Give the extent of all Plasmodium falciparum-infected red blood cells.
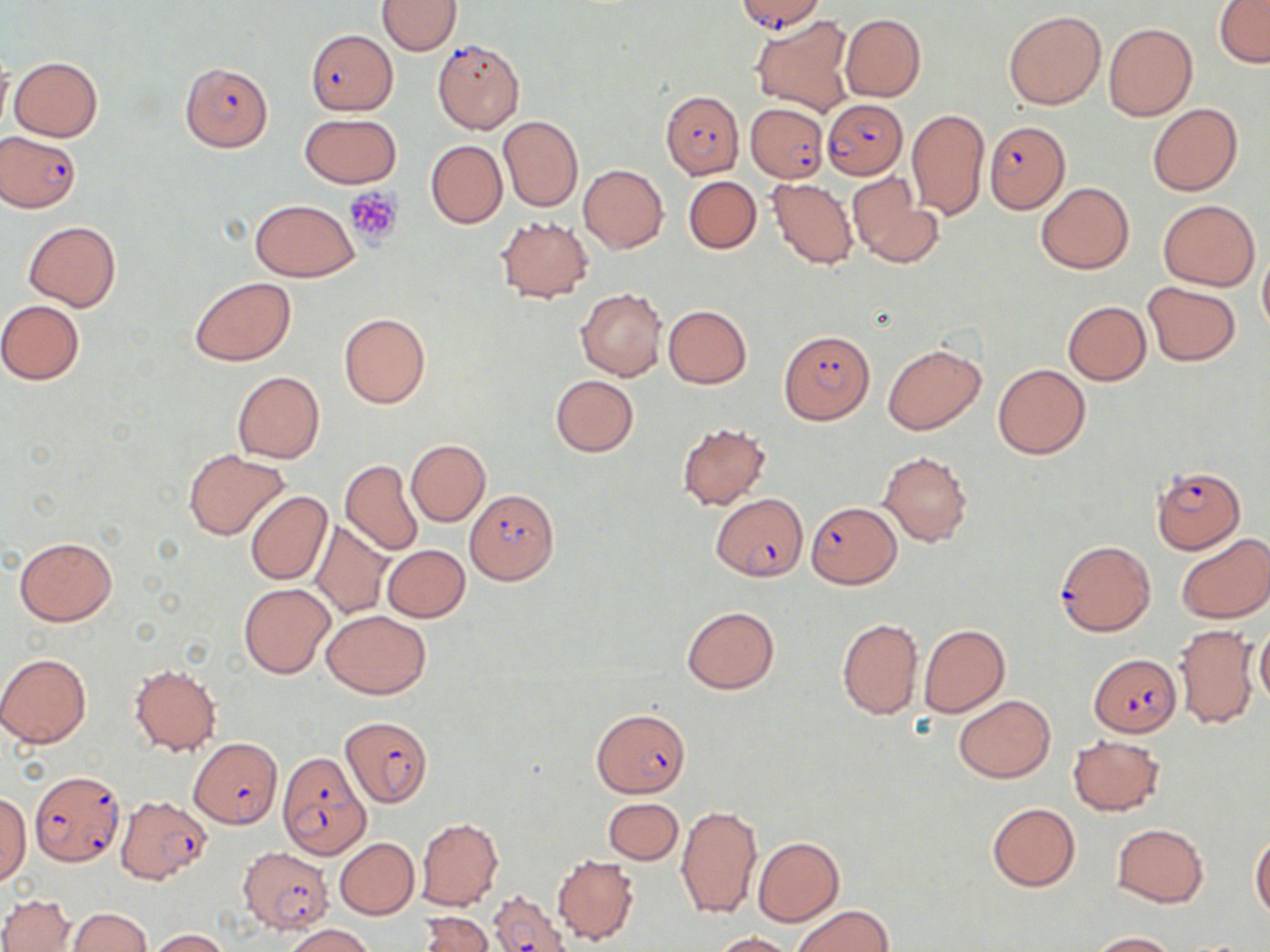

Approximate bounding boxes as [x1, y1, x2, y2] in pixels.
Plasmodium falciparum-infected red blood cells: [735, 0, 824, 34], [307, 29, 396, 115], [432, 37, 526, 134], [180, 62, 273, 151], [663, 89, 744, 180], [821, 98, 908, 179], [744, 102, 829, 182], [984, 120, 1070, 213], [0, 132, 82, 213], [778, 331, 874, 424], [1150, 466, 1245, 553], [464, 490, 558, 585], [710, 494, 807, 579], [806, 500, 901, 588], [1054, 540, 1155, 636], [1091, 653, 1180, 735], [590, 708, 690, 798], [340, 716, 433, 807], [189, 737, 282, 828], [276, 753, 371, 859], [28, 769, 126, 867], [115, 794, 212, 884], [237, 847, 334, 933], [487, 889, 570, 951].

Platelet locations: [344, 187, 404, 246]. Uninfected red blood cell locations: [378, 0, 460, 55], [1214, 0, 1269, 68], [1004, 11, 1106, 109], [839, 13, 925, 102], [754, 18, 851, 114], [1103, 21, 1197, 121], [10, 56, 103, 141], [1147, 103, 1242, 196], [907, 108, 989, 219], [299, 114, 402, 188], [498, 115, 583, 212], [425, 140, 507, 229], [578, 164, 668, 253], [847, 174, 940, 267], [683, 175, 761, 254], [768, 179, 857, 267], [1036, 181, 1134, 274], [249, 199, 359, 282], [1158, 200, 1260, 291], [496, 216, 594, 302], [23, 221, 120, 311], [1258, 249, 1270, 339], [190, 277, 295, 366], [1142, 281, 1242, 366], [575, 288, 666, 381], [0, 300, 85, 384], [1062, 301, 1152, 385], [663, 305, 751, 388], [339, 312, 430, 409], [883, 343, 984, 434], [993, 362, 1090, 459], [233, 371, 325, 464], [549, 375, 638, 457], [676, 423, 771, 510], [405, 439, 490, 526], [184, 449, 286, 541], [879, 451, 973, 546], [341, 460, 423, 556], [245, 491, 332, 584], [311, 520, 392, 618], [1175, 533, 1270, 623], [14, 536, 117, 627], [383, 545, 470, 622], [239, 583, 335, 679], [682, 605, 779, 693], [321, 610, 430, 699], [836, 617, 924, 721], [918, 623, 1009, 718], [1172, 624, 1257, 730], [1254, 626, 1270, 707], [0, 653, 91, 748], [129, 664, 222, 756], [953, 694, 1055, 783], [1067, 735, 1165, 815], [0, 793, 30, 884], [604, 798, 683, 864], [986, 802, 1080, 891], [676, 805, 762, 919], [415, 817, 504, 910], [1112, 823, 1209, 907], [1250, 836, 1270, 922], [335, 837, 419, 919], [753, 837, 843, 927], [552, 853, 639, 945], [0, 892, 75, 952], [791, 905, 893, 952], [65, 907, 152, 951], [418, 912, 493, 952], [284, 924, 375, 952], [149, 929, 233, 951], [709, 930, 797, 951], [1086, 931, 1181, 951]. Slide-level diagnosis: Plasmodium falciparum. Thin blood film. Single field of view. Image is 1270×952 pixels. May-Grünwald-Giemsa-stained preparation. Light microscopy. Captured at 1000x magnification.